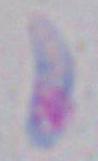

Summary:
  - Identification: Toxoplasma gondii
  - Magnification: 1000x
  - Modality: micrograph